Identify the cell.
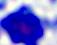
A leukocyte.

Summary:
  - Modality: micrograph
  - Magnification: 400x